Identify the parasite.
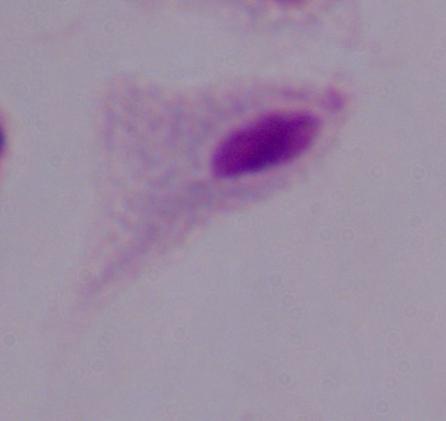

A trichomonad.

Summary:
  - Magnification: 1000x
  - Modality: photomicrograph